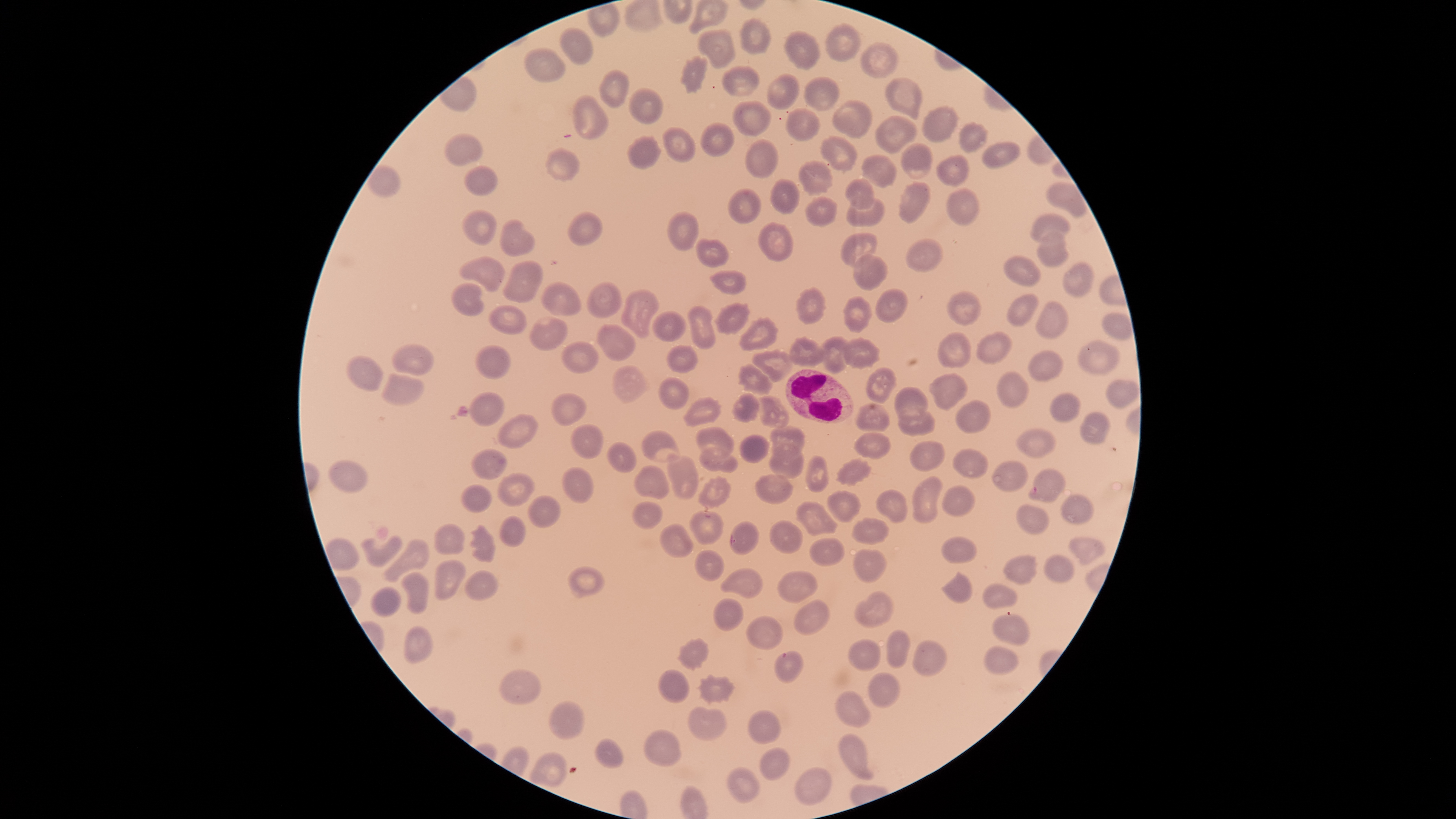
Approximate bounding boxes as {left, top, right, bottom} in pixels. Uninfected red blood cells: {739, 17, 772, 55}, {825, 23, 862, 63}, {559, 27, 593, 65}, {696, 29, 737, 70}, {784, 29, 822, 71}, {860, 41, 899, 79}, {524, 47, 566, 83}, {679, 54, 708, 94}, {722, 65, 762, 97}, {599, 69, 628, 110}, {766, 73, 800, 110}, {804, 76, 840, 112}, {885, 78, 922, 120}, {627, 87, 664, 124}, {572, 93, 609, 141}, {831, 98, 871, 138}, {732, 100, 773, 138}, {921, 103, 959, 144}, {785, 108, 822, 141}, {874, 115, 917, 154}, {699, 121, 735, 157}, {958, 121, 989, 155}, {662, 127, 695, 162}, {443, 132, 484, 167}, {818, 134, 857, 174}, {626, 136, 661, 169}, {744, 138, 778, 180}, {900, 141, 935, 179}, {981, 142, 1020, 170}, {545, 146, 580, 182}, {860, 154, 897, 189}, {934, 154, 970, 188}, {798, 159, 833, 197}, {365, 165, 402, 198}, {464, 165, 498, 197}, {770, 179, 800, 215}, {843, 179, 875, 210}, {897, 181, 931, 225}, {1045, 181, 1086, 218}, {727, 186, 761, 225}, {946, 186, 980, 227}, {804, 196, 839, 228}, {846, 198, 886, 228}, {462, 209, 498, 246}, {666, 209, 699, 252}, {567, 210, 603, 247}, {1029, 212, 1070, 244}, {499, 217, 535, 257}, {756, 221, 794, 262}, {1036, 229, 1069, 268}, {839, 232, 878, 267}, {695, 237, 730, 269}, {904, 237, 944, 274}, {853, 252, 888, 291}, {459, 255, 505, 293}, {1001, 255, 1041, 287}, {501, 258, 544, 304}, {1062, 261, 1093, 298}, {709, 269, 746, 295}, {540, 281, 582, 316}, {586, 281, 623, 319}, {450, 282, 485, 318}, {795, 286, 827, 325}, {874, 287, 908, 324}, {621, 288, 660, 339}, {946, 291, 982, 327}, {1007, 292, 1040, 327}, {842, 296, 872, 333}, {1035, 301, 1067, 341}, {714, 302, 751, 336}, {488, 304, 527, 335}, {687, 304, 717, 349}, {652, 310, 686, 343}, {528, 315, 568, 351}, {738, 316, 780, 351}, {596, 324, 635, 362}, {936, 331, 972, 368}, {975, 331, 1012, 366}, {819, 335, 850, 374}, {788, 336, 826, 367}, {842, 336, 881, 370}, {560, 339, 600, 374}, {1076, 339, 1120, 376}, {475, 343, 511, 380}, {666, 343, 698, 373}, {391, 344, 434, 376}, {752, 348, 793, 383}, {1027, 349, 1065, 382}, {345, 355, 383, 391}, {737, 363, 774, 398}, {612, 365, 650, 404}, {866, 366, 897, 404}, {995, 370, 1029, 410}, {928, 372, 968, 410}, {381, 373, 423, 408}, {657, 376, 688, 411}, {1105, 378, 1139, 409}, {894, 386, 928, 420}, {468, 391, 504, 427}, {550, 392, 587, 427}, {731, 392, 759, 423}, {1049, 392, 1081, 423}, {757, 394, 789, 428}, {682, 396, 723, 427}, {954, 400, 991, 434}, {854, 403, 890, 432}, {898, 410, 936, 437}, {1078, 411, 1110, 446}, {497, 412, 539, 450}, {569, 423, 604, 460}, {696, 425, 734, 458}, {770, 425, 805, 457}, {641, 429, 680, 464}, {1015, 429, 1056, 459}, {853, 432, 892, 460}, {739, 434, 769, 463}, {607, 439, 637, 474}, {909, 440, 946, 472}, {767, 442, 803, 480}, {699, 444, 738, 473}, {470, 447, 507, 481}, {952, 447, 989, 479}, {666, 453, 700, 500}, {805, 455, 829, 492}, {835, 457, 871, 487}, {327, 459, 368, 495}, {991, 460, 1028, 492}, {633, 464, 671, 501}, {561, 466, 595, 505}, {1027, 467, 1066, 504}, {497, 472, 535, 508}, {755, 474, 794, 505}, {698, 475, 731, 510}, {911, 476, 943, 526}, {459, 484, 492, 514}, {941, 485, 975, 518}, {827, 489, 862, 524}, {876, 489, 908, 524}, {1061, 493, 1094, 525}, {528, 495, 561, 529}, {794, 500, 838, 537}, {632, 501, 663, 531}, {1016, 504, 1050, 534}, {687, 510, 724, 546}, {498, 515, 527, 548}, {849, 517, 891, 545}, {769, 519, 804, 555}, {729, 520, 760, 555}, {433, 522, 467, 554}, {469, 523, 497, 564}, {658, 523, 694, 559}, {359, 535, 403, 568}, {1069, 535, 1106, 566}, {809, 537, 845, 566}, {941, 537, 978, 565}, {383, 538, 430, 584}, {852, 548, 887, 584}, {694, 549, 726, 581}, {1002, 554, 1038, 585}, {1043, 554, 1074, 583}, {434, 559, 467, 601}, {567, 565, 606, 599}, {719, 566, 765, 600}, {464, 569, 499, 602}, {775, 569, 819, 604}, {941, 571, 974, 605}, {401, 572, 430, 615}, {981, 581, 1019, 611}, {369, 586, 402, 617}, {853, 590, 894, 629}, {712, 598, 744, 633}, {793, 598, 830, 637}, {992, 611, 1031, 646}, {745, 615, 784, 650}, {401, 625, 433, 663}, {886, 629, 911, 669}, {674, 638, 710, 671}, {847, 638, 880, 672}, {912, 639, 949, 678}, {984, 645, 1018, 675}, {773, 651, 804, 684}, {499, 668, 542, 707}, {656, 670, 689, 705}, {867, 672, 901, 708}, {696, 673, 736, 706}, {835, 689, 872, 729}, {548, 700, 585, 740}, {687, 706, 728, 743}, {747, 709, 782, 746}, {643, 728, 682, 767}, {837, 733, 873, 780}, {593, 738, 626, 769}, {759, 747, 791, 781}, {725, 767, 761, 804}, {794, 767, 832, 807}. White blood cells: {785, 369, 854, 423}. Thin smear of blood. Image is 1456×819 pixels. Presence: no malaria parasites identified. One field of view of the specimen. Photographed with a smartphone camera through the microscope eyepiece. Giemsa-stained preparation. Circular visible region.